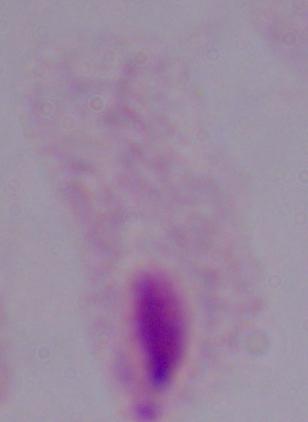

Micrograph. A trichomonad is seen. Captured at 1000x magnification.